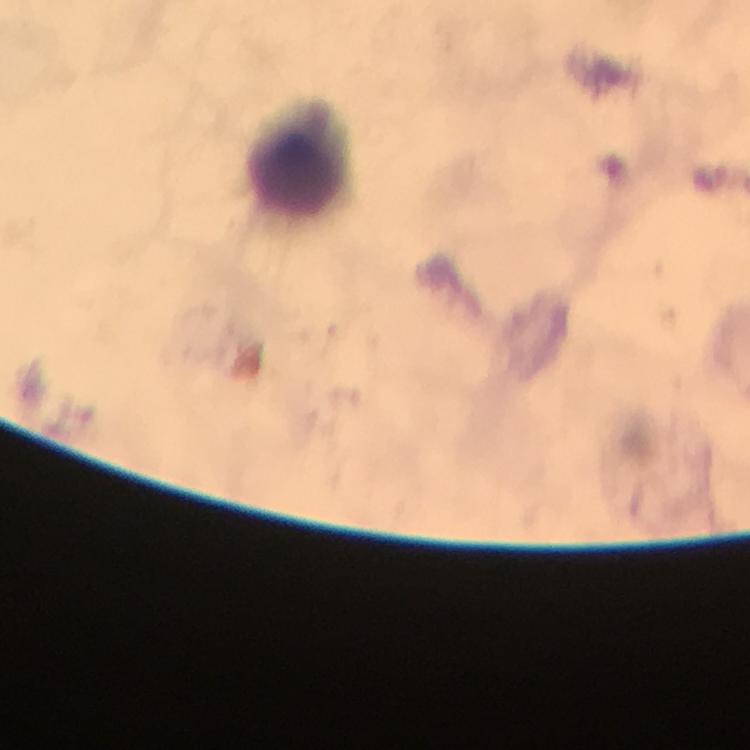
Approximate object centers, in pixels from the top-left corner. Leukocyte locations: (x=296, y=169). Smartphone photograph taken through a microscope. 100x magnification. Giemsa-stained preparation. Malaria parasites: none seen. Immersion oil was used. Cropped region of a single field of view. Image is 750×750 pixels. Thick blood film. From a diagnostic examination for malaria.